Report the malaria status of this cell.
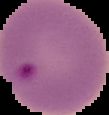

Parasitized.

Summary:
  - Preparation: thin blood film
  - Image size: 109×115 pixels
  - Image type: cell region segmented out of the field of view; surrounding area masked to black